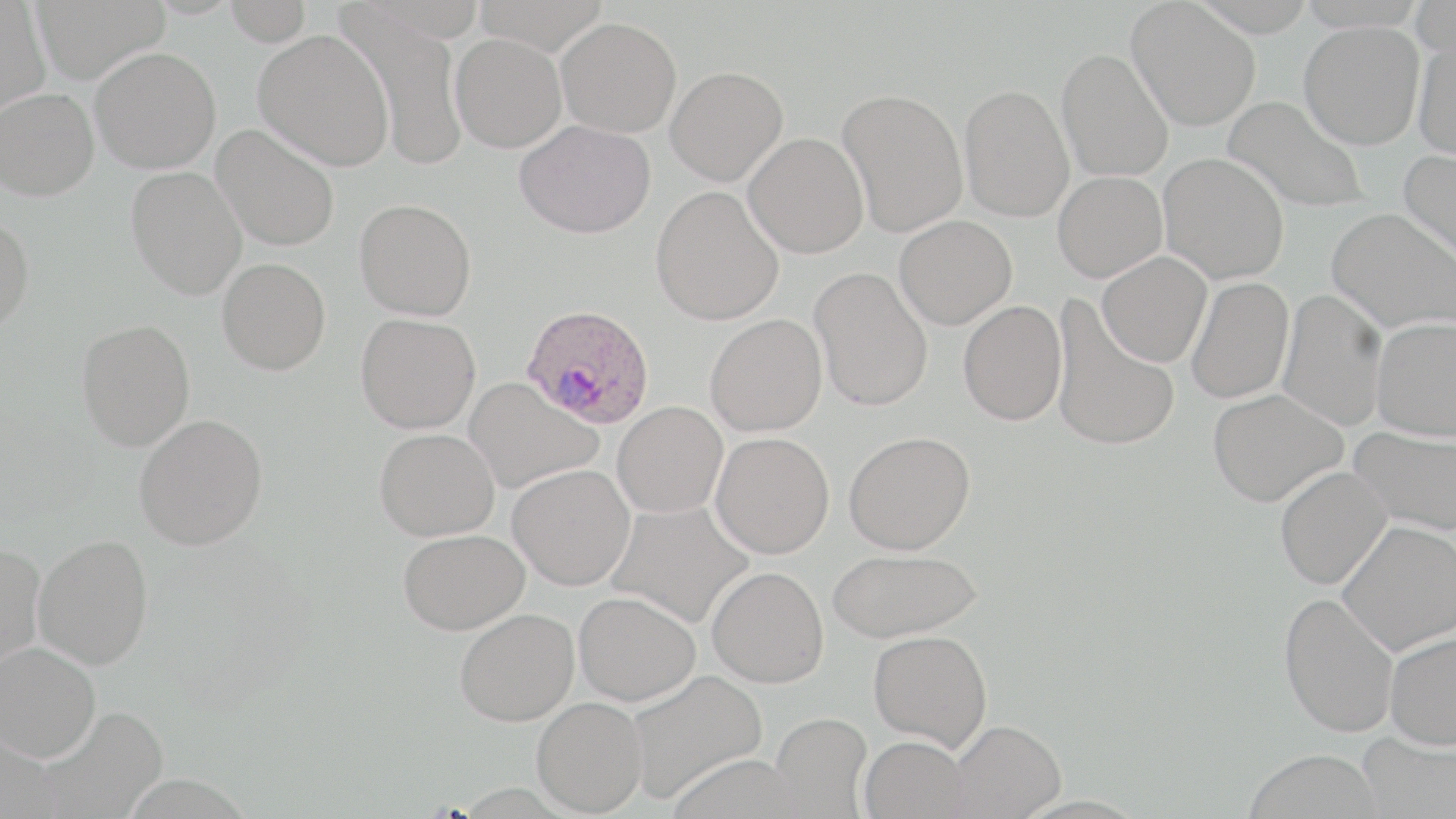
Summary:
  - Coordinate format: approximate bounding boxes as named x1/y1/x2/y2 corners in pixels
  - Uninfected red blood cell locations: (x1=30, y1=0, x2=170, y2=83), (x1=473, y1=0, x2=610, y2=55), (x1=1410, y1=0, x2=1456, y2=58), (x1=0, y1=1, x2=51, y2=116), (x1=223, y1=1, x2=314, y2=45), (x1=1127, y1=1, x2=1261, y2=131), (x1=335, y1=4, x2=469, y2=171), (x1=555, y1=16, x2=682, y2=137), (x1=1299, y1=21, x2=1424, y2=149), (x1=253, y1=29, x2=394, y2=170), (x1=450, y1=32, x2=567, y2=153), (x1=1413, y1=37, x2=1456, y2=162), (x1=90, y1=46, x2=222, y2=174), (x1=1056, y1=46, x2=1174, y2=182), (x1=665, y1=65, x2=788, y2=186), (x1=959, y1=84, x2=1074, y2=222), (x1=837, y1=87, x2=969, y2=237), (x1=0, y1=88, x2=100, y2=201), (x1=1223, y1=95, x2=1370, y2=214), (x1=514, y1=119, x2=656, y2=239), (x1=211, y1=123, x2=340, y2=251), (x1=743, y1=132, x2=869, y2=259), (x1=1399, y1=149, x2=1456, y2=268), (x1=1159, y1=153, x2=1289, y2=284), (x1=125, y1=166, x2=248, y2=300), (x1=1053, y1=171, x2=1167, y2=282), (x1=650, y1=185, x2=784, y2=325), (x1=355, y1=198, x2=477, y2=320), (x1=1326, y1=208, x2=1455, y2=335), (x1=0, y1=213, x2=34, y2=332), (x1=894, y1=215, x2=1016, y2=330), (x1=1097, y1=251, x2=1212, y2=367), (x1=218, y1=257, x2=330, y2=375), (x1=810, y1=267, x2=933, y2=411), (x1=1185, y1=276, x2=1294, y2=404), (x1=1277, y1=289, x2=1388, y2=432), (x1=1050, y1=297, x2=1181, y2=452), (x1=958, y1=299, x2=1067, y2=426), (x1=355, y1=313, x2=481, y2=434), (x1=705, y1=314, x2=827, y2=437), (x1=1371, y1=317, x2=1456, y2=440), (x1=76, y1=319, x2=195, y2=451), (x1=464, y1=378, x2=603, y2=494), (x1=1207, y1=388, x2=1349, y2=506), (x1=613, y1=401, x2=728, y2=518), (x1=134, y1=414, x2=268, y2=550), (x1=1350, y1=425, x2=1456, y2=536), (x1=374, y1=428, x2=499, y2=541), (x1=844, y1=430, x2=975, y2=555), (x1=710, y1=432, x2=834, y2=558), (x1=507, y1=464, x2=635, y2=590), (x1=1275, y1=466, x2=1392, y2=590), (x1=606, y1=499, x2=755, y2=628), (x1=1338, y1=520, x2=1456, y2=655), (x1=398, y1=529, x2=529, y2=634), (x1=32, y1=534, x2=154, y2=669), (x1=0, y1=543, x2=46, y2=672), (x1=827, y1=548, x2=982, y2=643), (x1=707, y1=567, x2=829, y2=688), (x1=574, y1=591, x2=701, y2=706), (x1=1278, y1=592, x2=1399, y2=737), (x1=454, y1=608, x2=579, y2=726), (x1=1384, y1=629, x2=1456, y2=749), (x1=869, y1=630, x2=992, y2=750), (x1=1, y1=642, x2=101, y2=761), (x1=625, y1=669, x2=767, y2=803), (x1=532, y1=696, x2=648, y2=816), (x1=36, y1=706, x2=169, y2=819), (x1=771, y1=712, x2=873, y2=817), (x1=949, y1=719, x2=1066, y2=818), (x1=0, y1=731, x2=60, y2=819), (x1=1357, y1=731, x2=1456, y2=819), (x1=860, y1=735, x2=970, y2=819), (x1=1244, y1=749, x2=1383, y2=819)
  - Plasmodium ovale-infected red blood cell locations: (x1=521, y1=304, x2=656, y2=430)
  - Slide-level diagnosis: Plasmodium ovale
  - Magnification: 1000x
  - Stain: May-Grünwald-Giemsa
  - Preparation: thin blood smear
  - Field of view: single
  - Image size: 1456×819 pixels
  - Modality: light microscopy